Assess this cell for malaria.
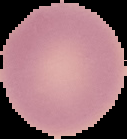

It is uninfected.

Summary:
  - Image type: cell region segmented out of the field of view; surrounding area masked to black
  - Preparation: thin blood smear
  - Image size: 127×139 pixels